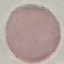
Result: no malaria parasites detected. Acquired by smartphone through the microscope eyepiece. Thin blood film. Automatically extracted cell patch, resized to 64 × 64 pixels. Giemsa-stained preparation.